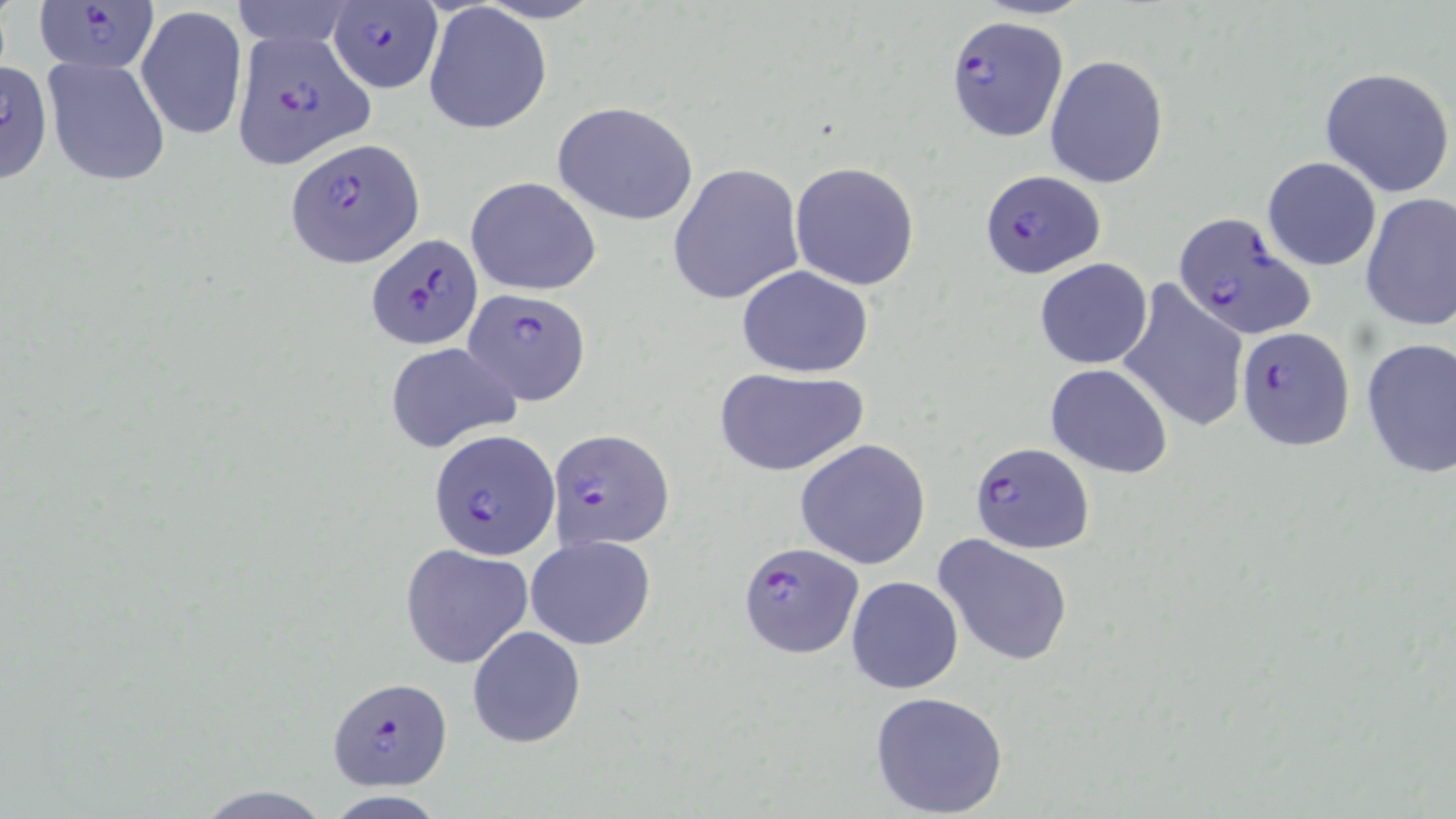

Summary:
  - Coordinate format: approximate bounding boxes as (x1,y1)-(x2,y2) corner pairs in pixels
  - Uninfected red blood cell locations: (230,0)-(357,50), (424,4)-(552,133), (136,5)-(248,139), (1044,54)-(1169,188), (42,58)-(172,187), (1,61)-(51,185), (1319,66)-(1455,197), (552,100)-(701,225), (1263,156)-(1381,271), (789,161)-(920,290), (667,162)-(805,306), (465,175)-(602,297), (1360,193)-(1456,331), (1034,258)-(1153,370), (736,265)-(875,378), (1118,278)-(1249,435), (1359,337)-(1456,479), (385,342)-(520,453), (1046,364)-(1173,478), (713,368)-(869,476), (794,440)-(932,569), (525,534)-(656,649), (932,534)-(1075,667), (399,543)-(533,669), (846,575)-(964,694), (465,625)-(587,748), (868,690)-(1009,817)
  - Plasmodium falciparum-infected red blood cell locations: (31,2)-(158,76), (327,2)-(442,93), (944,15)-(1068,142), (234,30)-(376,173), (289,137)-(419,267), (978,170)-(1105,279), (1171,211)-(1316,341), (366,232)-(481,350), (462,288)-(591,407), (1237,325)-(1354,450), (548,428)-(674,551), (431,430)-(559,561), (969,440)-(1095,555), (737,541)-(863,658), (326,677)-(452,789)
  - Slide-level diagnosis: Plasmodium falciparum
  - Image size: 1456×819 pixels
  - Modality: optical microscopy
  - Preparation: thin blood film
  - Magnification: 1000x
  - Field of view: one of a larger specimen
  - Stain: May-Grünwald-Giemsa